Report the malaria status of this cell.
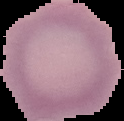

Uninfected.

From a thin blood film. Image is 124×121 pixels. Cell region segmented out of the field of view; the surrounding area is masked to black.